State which cell type is depicted.
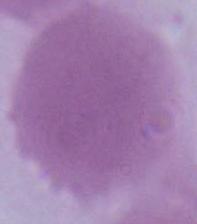
This is an erythrocyte.

modality: photomicrograph
magnification: 1000x